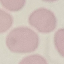
{
  "malaria_status": "uninfected",
  "capture": "smartphone camera at the microscope eyepiece",
  "preparation": "thin smear",
  "stain": "Giemsa",
  "image_type": "automatically extracted cell patch, resized to 64 × 64 pixels"
}